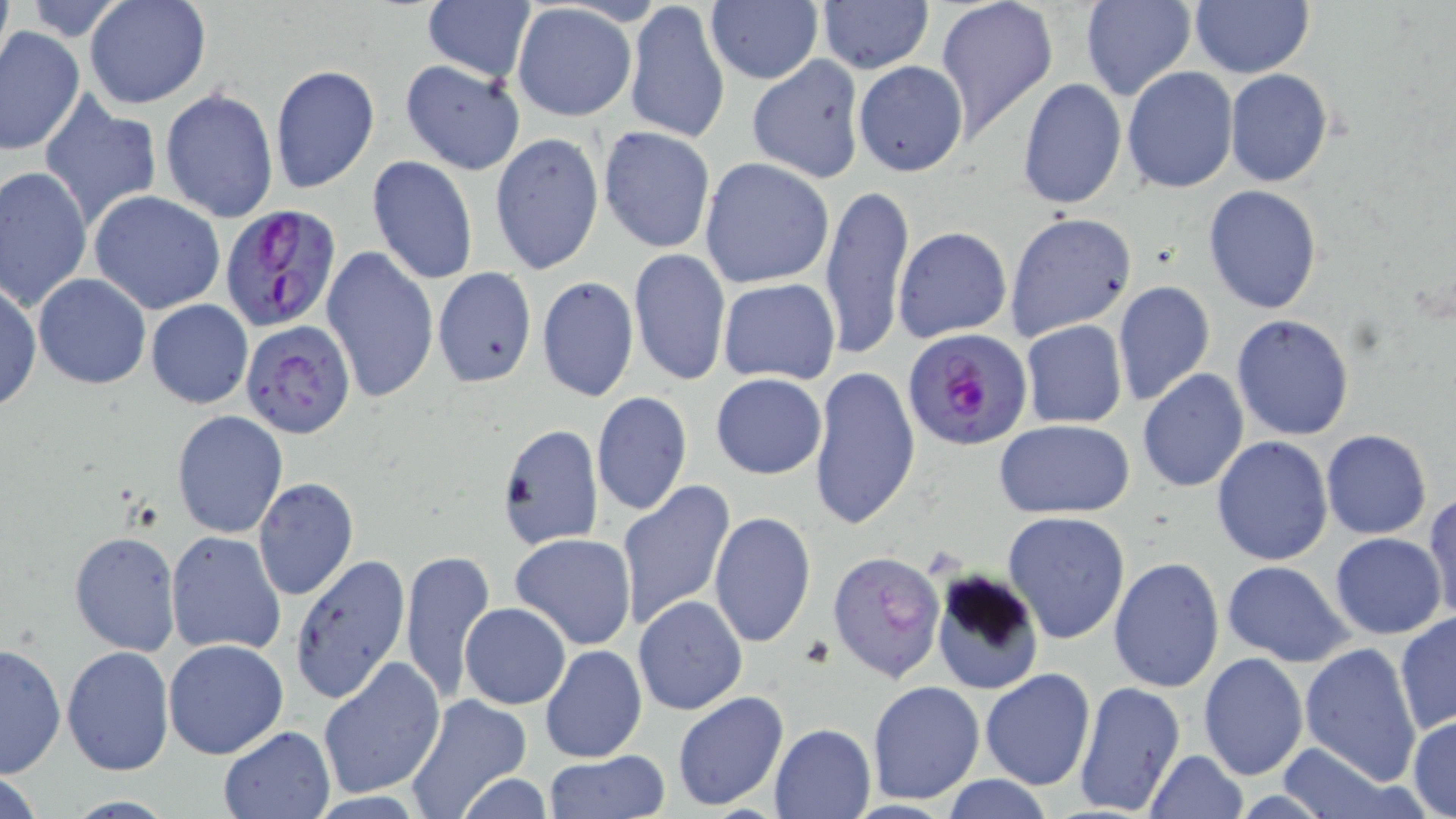
Approximate bounding boxes as named x1/y1/x2/y2 corners in pixels. Uninfected red blood cell locations: (x1=85, y1=0, x2=210, y2=108), (x1=421, y1=0, x2=536, y2=84), (x1=933, y1=0, x2=1057, y2=143), (x1=1080, y1=0, x2=1195, y2=102), (x1=626, y1=1, x2=732, y2=147), (x1=815, y1=1, x2=934, y2=73), (x1=1189, y1=1, x2=1314, y2=79), (x1=704, y1=2, x2=823, y2=87), (x1=510, y1=4, x2=635, y2=123), (x1=0, y1=27, x2=84, y2=154), (x1=746, y1=54, x2=866, y2=184), (x1=398, y1=59, x2=526, y2=175), (x1=853, y1=61, x2=968, y2=177), (x1=269, y1=63, x2=379, y2=197), (x1=1121, y1=66, x2=1237, y2=194), (x1=1225, y1=69, x2=1332, y2=187), (x1=1017, y1=78, x2=1126, y2=212), (x1=159, y1=89, x2=279, y2=221), (x1=39, y1=93, x2=163, y2=232), (x1=598, y1=125, x2=716, y2=253), (x1=489, y1=132, x2=604, y2=275), (x1=367, y1=156, x2=478, y2=285), (x1=700, y1=157, x2=834, y2=288), (x1=1, y1=167, x2=93, y2=312), (x1=819, y1=180, x2=915, y2=363), (x1=1203, y1=186, x2=1324, y2=314), (x1=88, y1=190, x2=225, y2=314), (x1=1004, y1=211, x2=1137, y2=340), (x1=894, y1=227, x2=1012, y2=343), (x1=320, y1=246, x2=437, y2=408), (x1=628, y1=248, x2=731, y2=387), (x1=432, y1=267, x2=537, y2=389), (x1=34, y1=274, x2=151, y2=389), (x1=537, y1=276, x2=639, y2=402), (x1=1, y1=277, x2=41, y2=414), (x1=716, y1=278, x2=841, y2=385), (x1=1112, y1=280, x2=1217, y2=407), (x1=146, y1=299, x2=253, y2=410), (x1=1232, y1=313, x2=1355, y2=441), (x1=1021, y1=319, x2=1127, y2=427), (x1=809, y1=363, x2=921, y2=532), (x1=1137, y1=369, x2=1250, y2=493), (x1=710, y1=373, x2=827, y2=480), (x1=592, y1=392, x2=691, y2=515), (x1=173, y1=410, x2=287, y2=538), (x1=995, y1=420, x2=1137, y2=519), (x1=497, y1=423, x2=603, y2=549), (x1=1321, y1=430, x2=1433, y2=540), (x1=1210, y1=436, x2=1334, y2=566), (x1=253, y1=477, x2=359, y2=601), (x1=616, y1=478, x2=736, y2=631), (x1=1425, y1=494, x2=1456, y2=628), (x1=708, y1=511, x2=816, y2=651), (x1=1002, y1=512, x2=1130, y2=644), (x1=167, y1=530, x2=287, y2=657), (x1=69, y1=531, x2=180, y2=656), (x1=1330, y1=532, x2=1446, y2=639), (x1=509, y1=533, x2=637, y2=650), (x1=400, y1=548, x2=495, y2=705), (x1=829, y1=550, x2=945, y2=682), (x1=291, y1=555, x2=414, y2=709), (x1=1108, y1=556, x2=1225, y2=693), (x1=1222, y1=562, x2=1352, y2=667), (x1=929, y1=568, x2=1043, y2=699), (x1=633, y1=594, x2=748, y2=716), (x1=461, y1=602, x2=570, y2=709), (x1=1395, y1=615, x2=1455, y2=736), (x1=164, y1=638, x2=289, y2=758), (x1=1, y1=641, x2=65, y2=780), (x1=1299, y1=641, x2=1421, y2=785), (x1=540, y1=643, x2=647, y2=762), (x1=62, y1=645, x2=172, y2=774), (x1=1197, y1=652, x2=1308, y2=781), (x1=318, y1=657, x2=445, y2=798), (x1=979, y1=669, x2=1095, y2=791), (x1=1072, y1=678, x2=1184, y2=817), (x1=865, y1=680, x2=985, y2=805), (x1=672, y1=690, x2=790, y2=813), (x1=403, y1=695, x2=533, y2=817), (x1=1408, y1=713, x2=1456, y2=817), (x1=769, y1=723, x2=875, y2=818), (x1=219, y1=727, x2=335, y2=817), (x1=1271, y1=740, x2=1409, y2=819), (x1=1145, y1=749, x2=1248, y2=818), (x1=543, y1=750, x2=671, y2=819), (x1=0, y1=764, x2=48, y2=819), (x1=454, y1=773, x2=555, y2=819), (x1=937, y1=776, x2=1059, y2=817). Platelet locations: (x1=794, y1=634, x2=836, y2=669). Plasmodium falciparum-infected red blood cell locations: (x1=220, y1=207, x2=345, y2=333), (x1=243, y1=321, x2=356, y2=440), (x1=903, y1=327, x2=1033, y2=452). Slide-level diagnosis: Plasmodium falciparum. May-Grünwald-Giemsa-stained preparation. Thin blood smear. Image is 1456×819 pixels. 1000x magnification. Optical microscopy. One field of a larger specimen.